Outline each uninfected red blood cell.
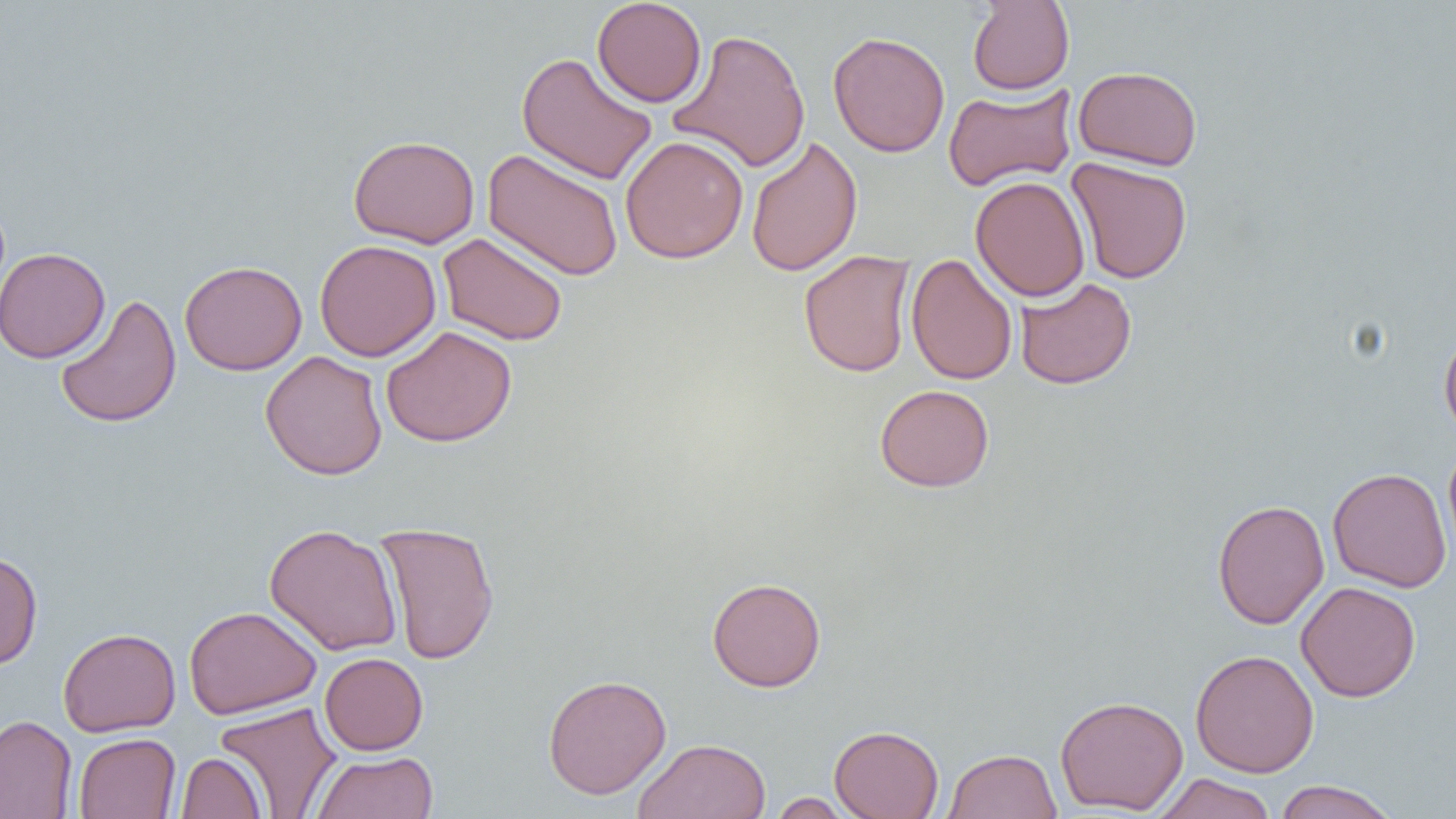

Approximate bounding boxes as (x1, y1, x2, y2) in pixels.
Uninfected red blood cells: (592, 0, 707, 107), (967, 1, 1075, 95), (668, 28, 812, 172), (828, 31, 950, 158), (516, 51, 658, 186), (1073, 65, 1203, 171), (943, 83, 1077, 192), (348, 134, 480, 248), (620, 135, 749, 264), (745, 136, 863, 278), (482, 149, 624, 282), (1065, 157, 1193, 284), (970, 176, 1090, 302), (437, 232, 568, 347), (314, 239, 441, 362), (0, 247, 110, 363), (799, 250, 916, 378), (906, 253, 1018, 386), (179, 260, 307, 375), (1014, 277, 1137, 390), (54, 293, 182, 429), (381, 325, 518, 447), (1439, 326, 1456, 442), (260, 351, 388, 480), (875, 384, 995, 492), (1442, 440, 1456, 568), (1327, 467, 1452, 593), (1212, 498, 1329, 630), (375, 520, 500, 665), (264, 523, 403, 656), (0, 550, 43, 670), (707, 576, 826, 691), (1296, 581, 1421, 702), (184, 606, 321, 719), (58, 627, 181, 736), (1190, 649, 1319, 777), (319, 652, 429, 755), (543, 674, 672, 799), (1055, 694, 1188, 815), (214, 701, 342, 818), (0, 715, 77, 819), (829, 725, 944, 819), (73, 732, 181, 818), (633, 738, 772, 819), (943, 748, 1062, 819), (311, 751, 439, 819), (175, 752, 267, 818), (1152, 773, 1277, 819), (1273, 780, 1400, 819), (768, 792, 856, 818).

slide_level_diagnosis: negative for blood parasites
image_size: 1456×819 pixels
field_of_view: one of a larger specimen
modality: optical microscopy
preparation: thin blood smear
magnification: 1000x